Classify this cell by malaria status.
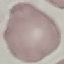
Uninfected.

Giemsa-stained preparation. Thin blood smear. Acquired by smartphone through the microscope eyepiece. Automatically extracted cell patch, resized to 64 × 64 pixels.